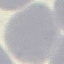
Summary:
  - Result: no malaria parasites detected
  - Image type: automatically extracted cell patch, resized to 64 × 64 pixels
  - Preparation: thin blood film
  - Capture: smartphone camera at the microscope eyepiece
  - Stain: Giemsa